Assess this cell for malaria.
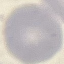

Uninfected.

Summary:
  - Image type: cell patch, automatically extracted from a larger field of view and resized to 64 × 64 pixels
  - Preparation: thin blood smear
  - Capture: smartphone through the microscope eyepiece
  - Stain: Giemsa